State the preparation type.
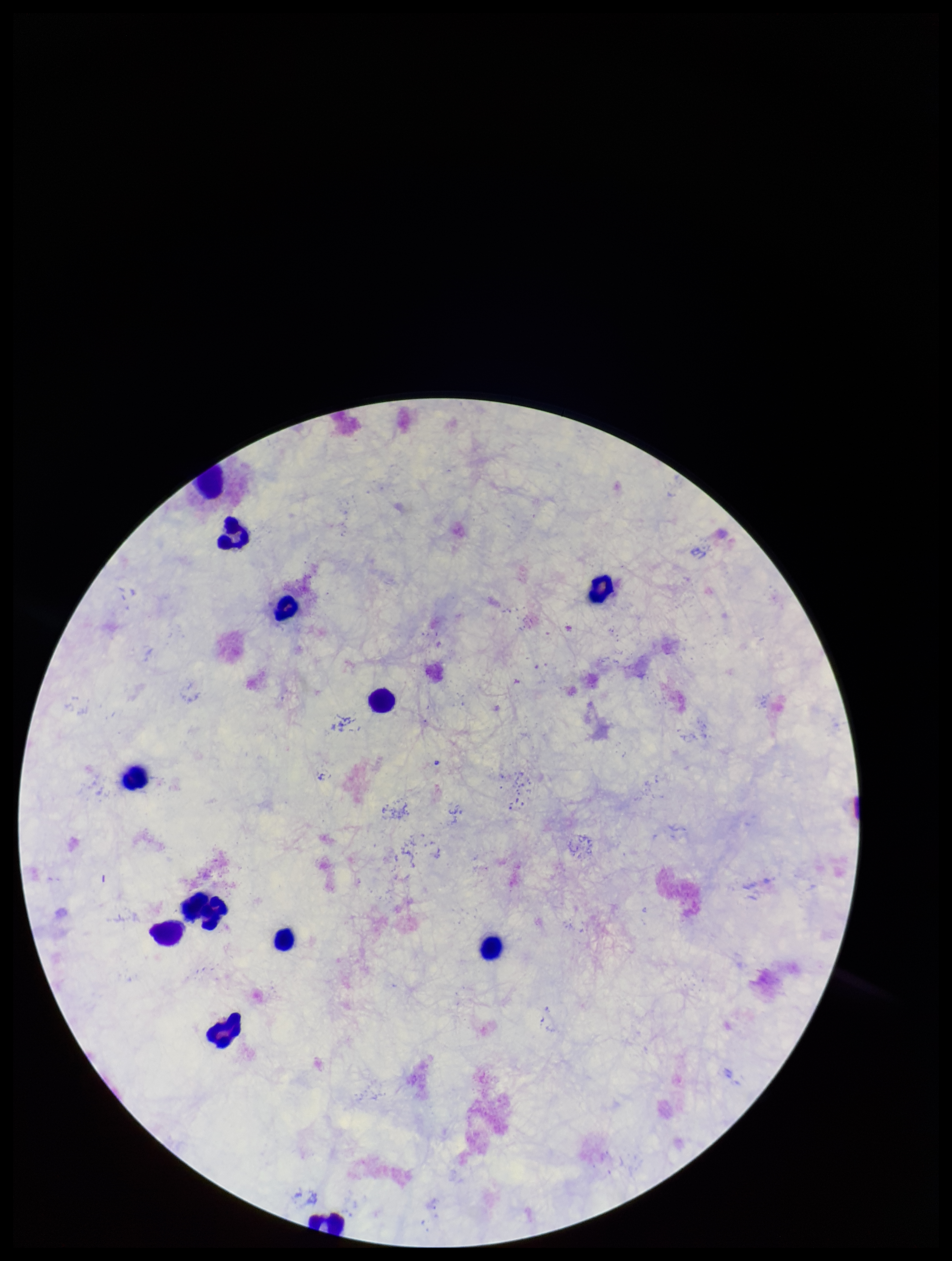

A thick smear.

Summary:
  - Patient malaria status: negative
  - Parasite count: 0
  - Field of view: one from this slide
  - Plasmodium parasites: none seen
  - Stain: Giemsa
  - Image size: 952×1261 pixels
  - Capture: smartphone photograph through the microscope eyepiece
  - Leukocyte count: 12